Locate and identify every blood parasite.
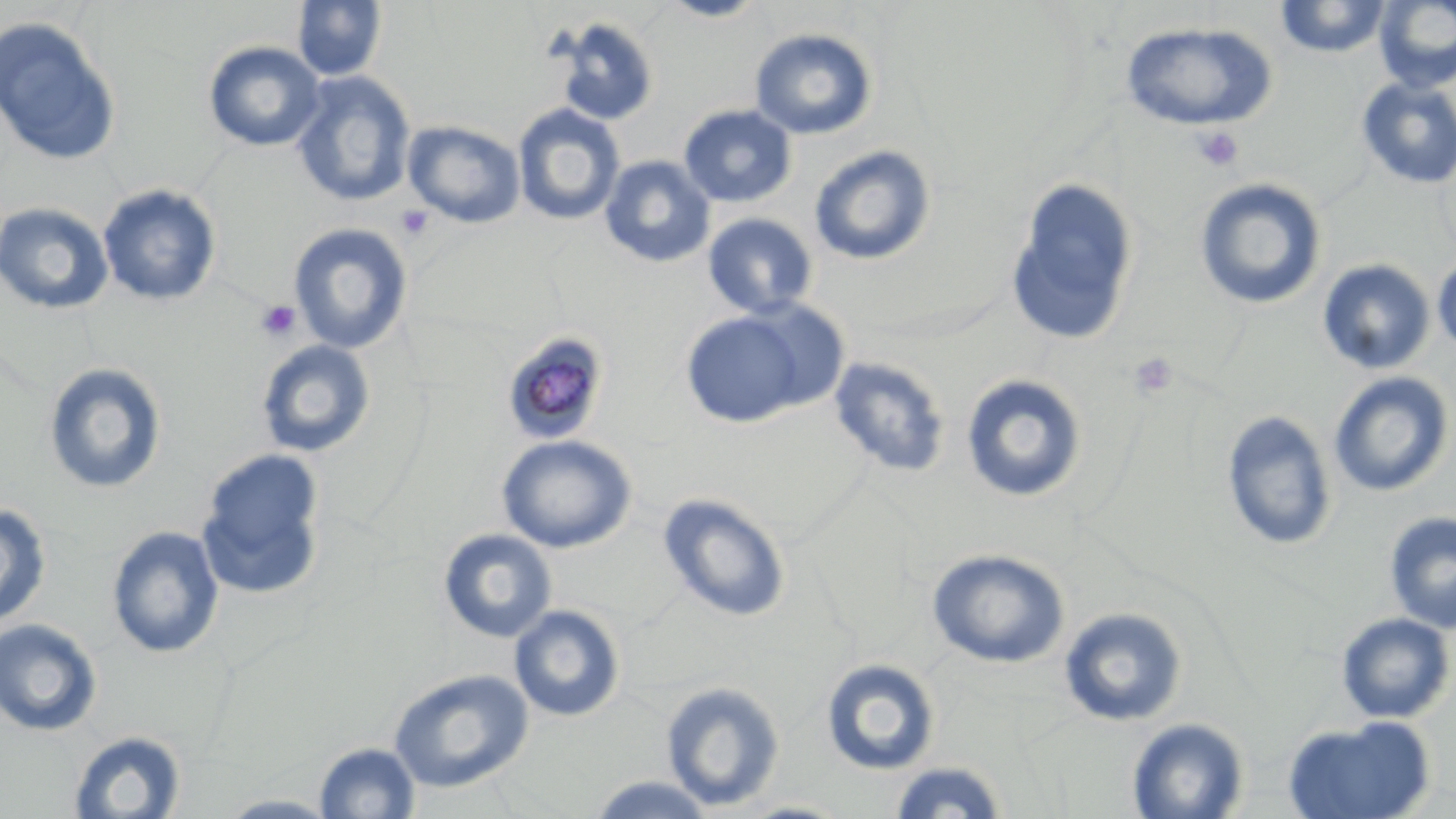

Approximate bounding boxes as [x1, y1, x2, y2] in pixels.
Plasmodium malariae-infected red blood cells: [499, 330, 612, 446].
No Plasmodium falciparum, Plasmodium ovale, Plasmodium vivax, Babesia divergens, or Trypanosoma brucei observed.

slide-level diagnosis = Plasmodium malariae
field of view = single
platelet locations = approximate bounding boxes as [x1, y1, x2, y2] in pixels: [1193, 127, 1245, 172], [396, 205, 434, 241], [255, 299, 301, 342], [1128, 351, 1179, 399]
stain = May-Grünwald-Giemsa
preparation = thin blood film
uninfected red blood cell locations = approximate bounding boxes as [x1, y1, x2, y2] in pixels: [655, 0, 772, 22], [1274, 0, 1392, 58], [1373, 0, 1456, 93], [291, 1, 387, 82], [0, 16, 122, 167], [549, 17, 660, 127], [1119, 21, 1278, 132], [749, 27, 879, 140], [202, 41, 326, 152], [290, 71, 417, 207], [1355, 77, 1456, 189], [512, 104, 625, 226], [678, 104, 798, 208], [403, 120, 526, 228], [808, 145, 936, 266], [599, 155, 716, 269], [1005, 176, 1140, 346], [1194, 177, 1327, 310], [97, 184, 222, 307], [0, 202, 115, 316], [702, 213, 818, 320], [288, 223, 412, 353], [1432, 252, 1456, 356], [1317, 259, 1436, 376], [733, 300, 853, 414], [680, 309, 812, 428], [255, 339, 375, 458], [828, 356, 951, 478], [42, 362, 167, 495], [1328, 371, 1454, 498], [960, 373, 1088, 503], [1221, 410, 1338, 551], [496, 434, 638, 553], [195, 449, 328, 600], [657, 492, 792, 623], [0, 501, 52, 630], [1384, 512, 1456, 632], [106, 524, 225, 659], [437, 528, 557, 644], [927, 548, 1070, 669], [509, 604, 626, 722], [1058, 606, 1188, 727], [1335, 612, 1455, 724], [0, 618, 103, 737], [821, 657, 941, 776], [388, 668, 534, 794], [660, 680, 785, 811], [1125, 717, 1249, 818], [1282, 718, 1436, 818], [68, 729, 188, 818], [313, 741, 421, 819], [886, 760, 1011, 819], [582, 774, 719, 818], [216, 793, 344, 818]
magnification = 1000x
image size = 1456×819 pixels
modality = optical microscopy